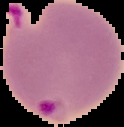
Summary:
  - Result: Plasmodium parasites detected
  - Preparation: thin blood film
  - Image type: segmented cell region on a black background
  - Image size: 124×127 pixels